Identify the parasite.
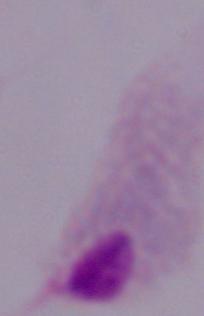
A trichomonad.

{
  "modality": "micrograph",
  "magnification": "1000x"
}